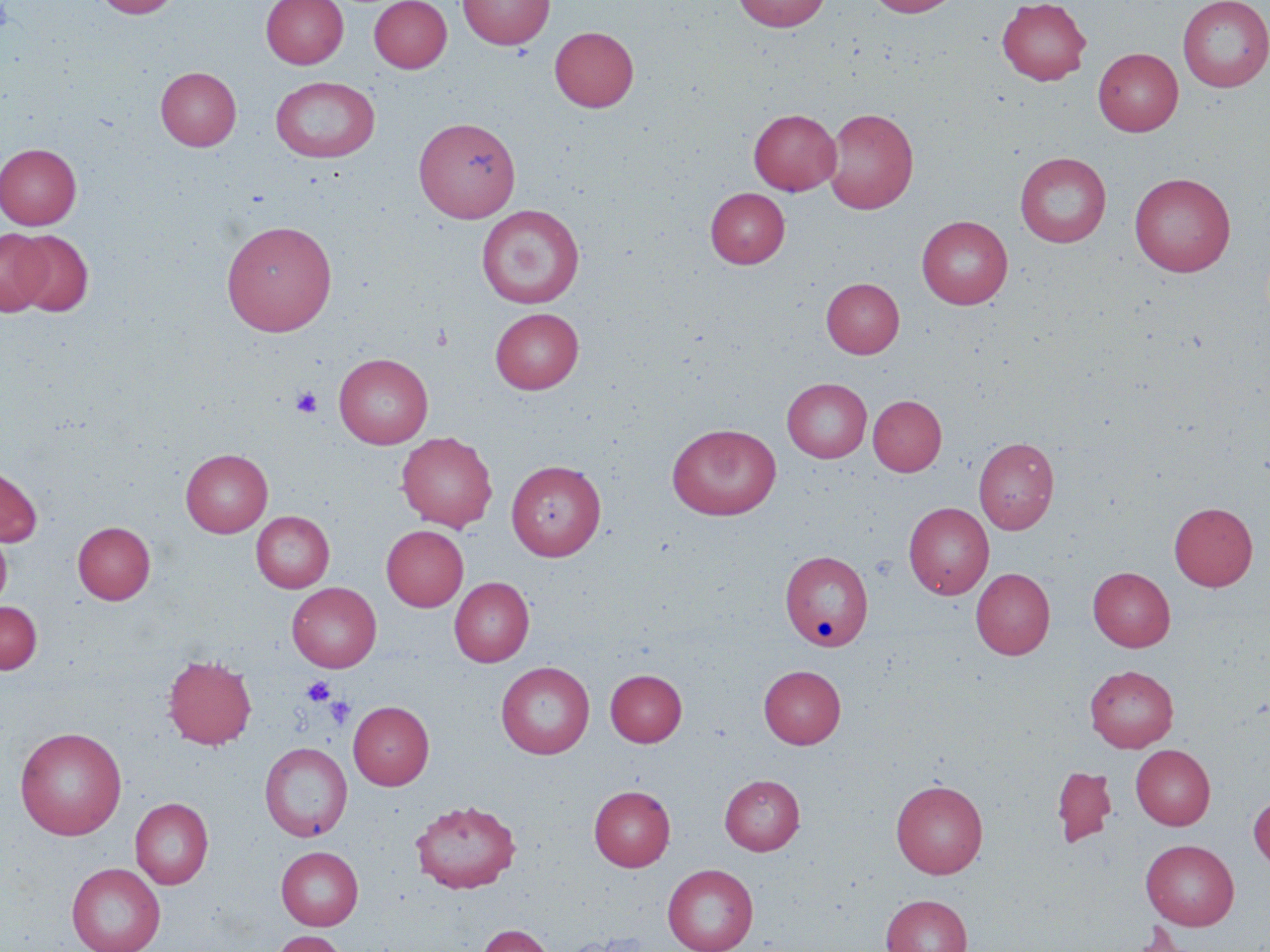

Approximate bounding boxes as [x1, y1, x2, y2] in pixels. Uninfected red blood cell locations: [94, 0, 181, 18], [261, 0, 348, 68], [369, 0, 452, 72], [458, 0, 554, 50], [732, 0, 831, 32], [867, 0, 961, 17], [997, 0, 1091, 85], [1178, 0, 1270, 91], [550, 26, 638, 112], [1093, 47, 1183, 136], [155, 67, 241, 150], [270, 76, 381, 163], [823, 107, 919, 214], [748, 109, 841, 195], [413, 116, 521, 222], [0, 143, 82, 229], [1015, 152, 1112, 247], [1130, 172, 1235, 276], [706, 187, 789, 268], [477, 205, 584, 308], [916, 215, 1013, 309], [222, 220, 337, 336], [0, 229, 52, 315], [12, 230, 93, 317], [821, 277, 904, 358], [490, 308, 584, 393], [334, 353, 433, 448], [782, 378, 871, 462], [868, 395, 947, 476], [668, 423, 781, 520], [396, 432, 497, 531], [974, 437, 1059, 534], [180, 448, 272, 537], [507, 459, 606, 560], [0, 464, 43, 547], [904, 502, 994, 599], [1169, 502, 1257, 591], [251, 511, 334, 593], [73, 522, 155, 604], [381, 525, 468, 611], [0, 526, 12, 610], [780, 549, 873, 652], [1088, 567, 1175, 651], [971, 568, 1055, 659], [450, 577, 534, 666], [287, 582, 381, 672], [0, 601, 42, 674], [163, 654, 257, 750], [495, 661, 594, 759], [759, 665, 846, 748], [1085, 665, 1178, 752], [605, 669, 687, 746], [348, 701, 434, 789], [15, 726, 127, 840], [259, 741, 352, 842], [1131, 744, 1215, 829], [1051, 765, 1117, 847], [720, 774, 805, 854], [891, 779, 988, 878], [589, 785, 674, 870], [1249, 793, 1270, 871], [130, 797, 214, 889], [410, 798, 521, 893], [1140, 839, 1239, 930], [276, 846, 363, 930], [66, 863, 165, 952], [662, 863, 759, 952], [881, 894, 971, 952], [1122, 921, 1210, 952], [478, 924, 554, 952], [268, 930, 349, 952]. Platelet locations: [291, 386, 322, 418], [302, 677, 335, 706], [313, 680, 349, 714], [323, 694, 356, 728]. Slide-level diagnosis: no evidence of blood parasites. One field of a larger specimen. Captured at 1000x magnification. Thin blood film. Image is 1270×952 pixels. May-Grünwald-Giemsa-stained preparation. Light microscopy.